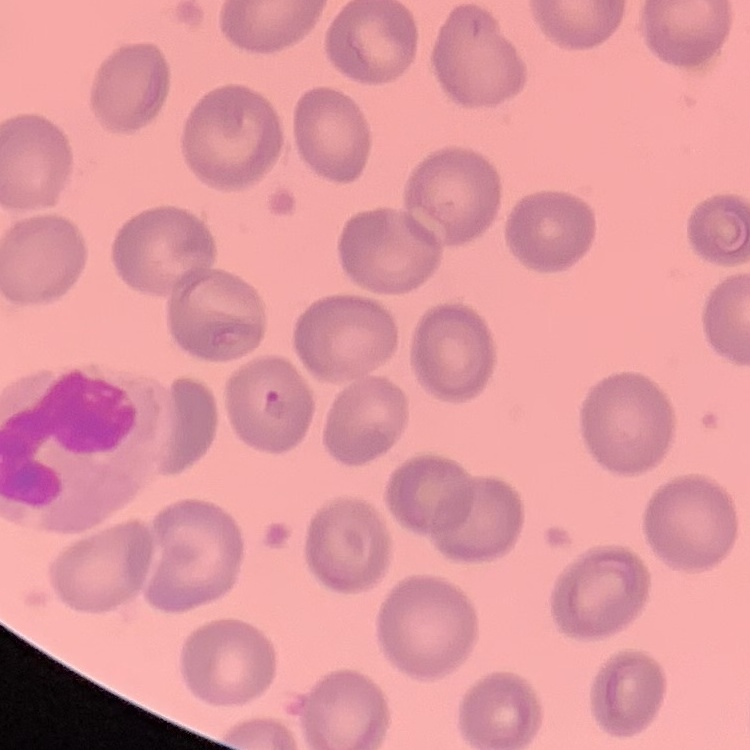

erythrocyte morphology = no rouleaux formation
stain = Field's or Giemsa
preparation = thin blood film
image type = one tile cut from a larger photomicrograph